Locate every blood parasite and identify its species.
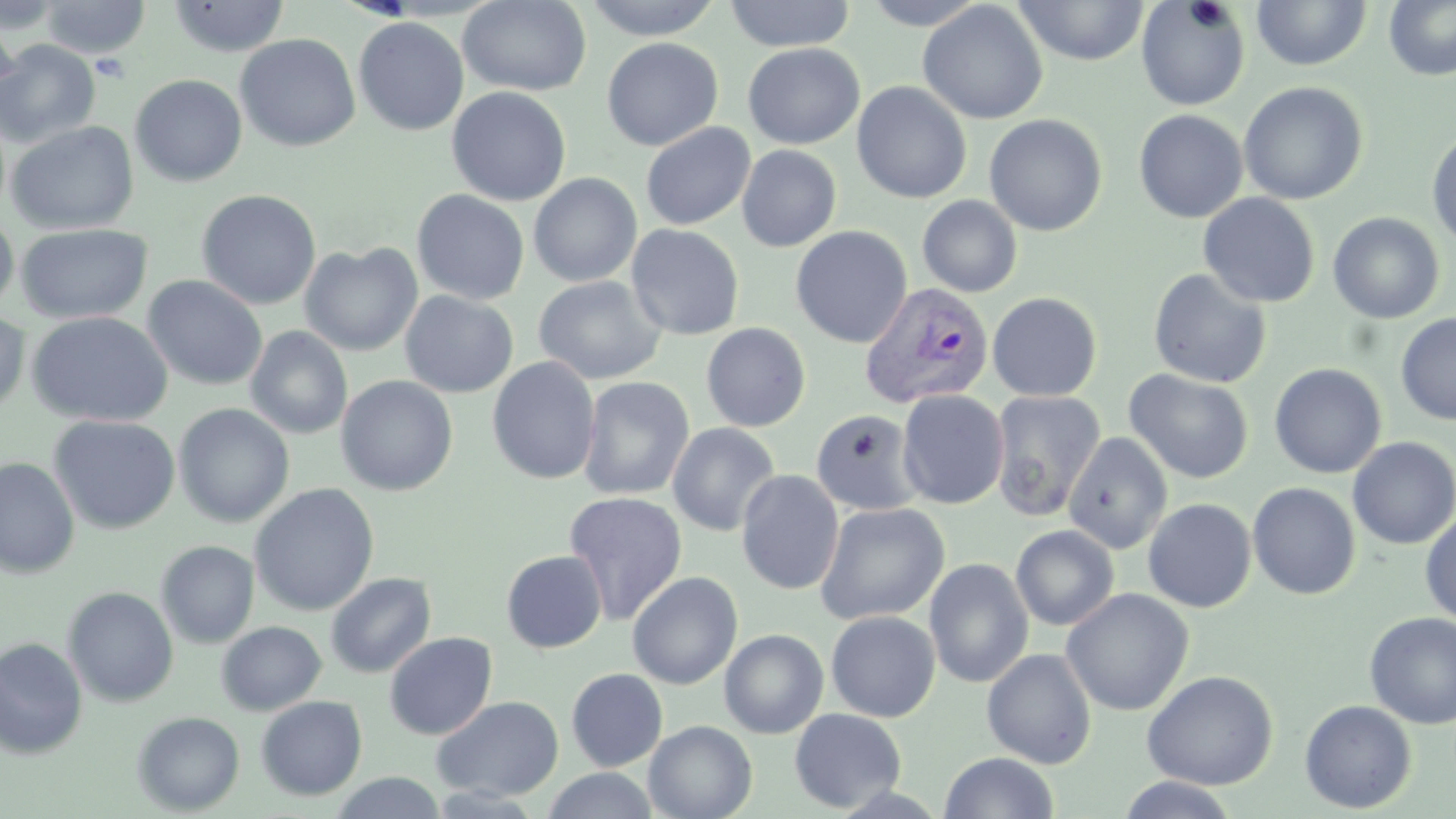
Approximate bounding boxes as (x1, y1, x2, y2) in pixels.
Plasmodium vivax-infected red blood cells: (860, 282, 993, 409).
No Plasmodium falciparum, Plasmodium ovale, Plasmodium malariae, Babesia divergens, or Trypanosoma brucei observed.

Summary:
  - Uninfected red blood cell locations: (0, 0, 66, 34), (40, 0, 150, 58), (167, 0, 290, 57), (457, 0, 592, 97), (581, 0, 726, 40), (723, 0, 856, 52), (859, 0, 991, 30), (1384, 0, 1456, 81), (917, 1, 1048, 124), (1013, 1, 1150, 66), (1135, 1, 1251, 111), (1251, 1, 1373, 71), (0, 10, 21, 109), (353, 17, 469, 136), (235, 34, 361, 153), (601, 37, 723, 151), (0, 40, 101, 148), (742, 43, 865, 149), (129, 74, 247, 187), (851, 81, 972, 204), (1239, 81, 1369, 206), (447, 86, 571, 206), (1133, 109, 1248, 224), (983, 114, 1108, 236), (6, 121, 139, 234), (640, 122, 756, 231), (1426, 127, 1456, 249), (736, 145, 842, 252), (528, 172, 643, 288), (195, 189, 321, 310), (411, 189, 530, 305), (1197, 193, 1320, 308), (917, 195, 1023, 297), (0, 212, 19, 315), (1327, 212, 1445, 324), (16, 223, 153, 325), (626, 224, 745, 341), (790, 225, 912, 348), (299, 242, 423, 356), (1148, 268, 1271, 389), (142, 275, 268, 392), (532, 275, 666, 386), (399, 291, 519, 398), (987, 292, 1102, 401), (27, 311, 173, 427), (0, 312, 30, 416), (1395, 313, 1456, 425), (701, 322, 811, 432), (245, 325, 353, 440), (486, 356, 600, 485), (1269, 363, 1387, 479), (1124, 369, 1254, 484), (335, 375, 458, 496), (577, 376, 695, 501), (896, 390, 1010, 509), (989, 390, 1106, 520), (173, 403, 295, 528), (811, 409, 923, 516), (48, 415, 181, 534), (667, 422, 781, 537), (1062, 432, 1173, 555), (1347, 436, 1456, 550), (0, 457, 80, 578), (736, 469, 844, 595), (1247, 482, 1361, 600), (249, 483, 379, 616), (562, 491, 688, 625), (1142, 498, 1257, 612), (814, 502, 950, 625), (1420, 511, 1455, 627), (1011, 525, 1120, 631), (156, 540, 259, 649), (501, 550, 607, 653), (923, 558, 1034, 688), (627, 571, 743, 690), (325, 572, 436, 678), (62, 586, 179, 707), (1060, 588, 1194, 716), (825, 610, 940, 722), (1363, 612, 1456, 729), (216, 621, 326, 715), (719, 621, 941, 731), (719, 628, 829, 739), (384, 631, 498, 740), (0, 637, 88, 759), (982, 648, 1097, 769), (566, 668, 668, 772), (1142, 669, 1278, 790), (255, 696, 367, 801), (431, 696, 564, 801), (1299, 699, 1416, 813), (789, 708, 907, 813), (131, 711, 245, 815), (644, 720, 757, 819), (939, 752, 1059, 818), (541, 768, 659, 819), (329, 772, 447, 818), (1115, 776, 1241, 818)
  - Slide-level diagnosis: Plasmodium vivax
  - Magnification: 1000x
  - Stain: May-Grünwald-Giemsa
  - Preparation: thin blood smear
  - Field of view: single
  - Image size: 1456×819 pixels
  - Modality: optical microscopy